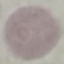
{
  "malaria_status": "uninfected",
  "stain": "Giemsa",
  "capture": "smartphone through the microscope eyepiece",
  "image_type": "automatically extracted cell patch, resized to 64 × 64 pixels",
  "preparation": "thin blood smear"
}